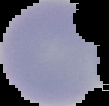
image type = cell region segmented out of the field of view; surrounding area masked to black
result = no malaria parasites detected
image size = 109×106 pixels
preparation = thin blood film